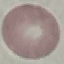

Result: no malaria parasites detected. Automatically extracted cell patch, resized to 64 × 64 pixels. Giemsa stain. Photographed with a smartphone camera at the microscope eyepiece. Thin blood film.